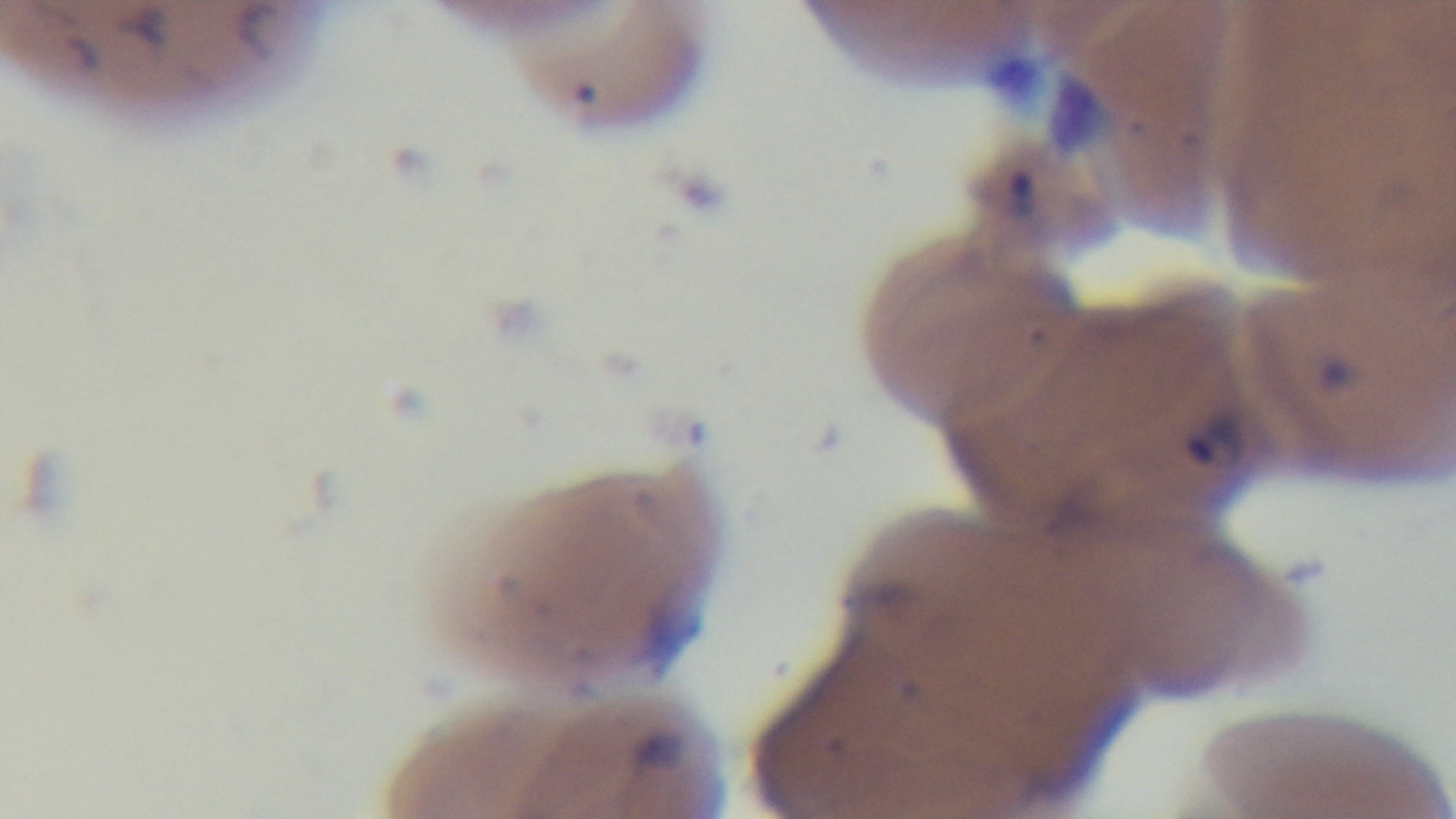 Giemsa-stained. Single field of view. Preparation: thin. 100x oil-immersion objective. Malaria status: infected. Light microscopy. Captured with a mounted 4K digital camera.